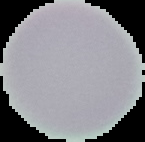
image size = 145×142 pixels
preparation = thin blood smear
malaria status = uninfected
image type = cell region segmented out of the field of view; surrounding area masked to black